Report the malaria status of this cell.
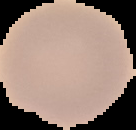

It is uninfected.

{
  "preparation": "thin blood film",
  "image_size": "136×130 pixels",
  "image_type": "segmented cell region with the area outside set to black"
}